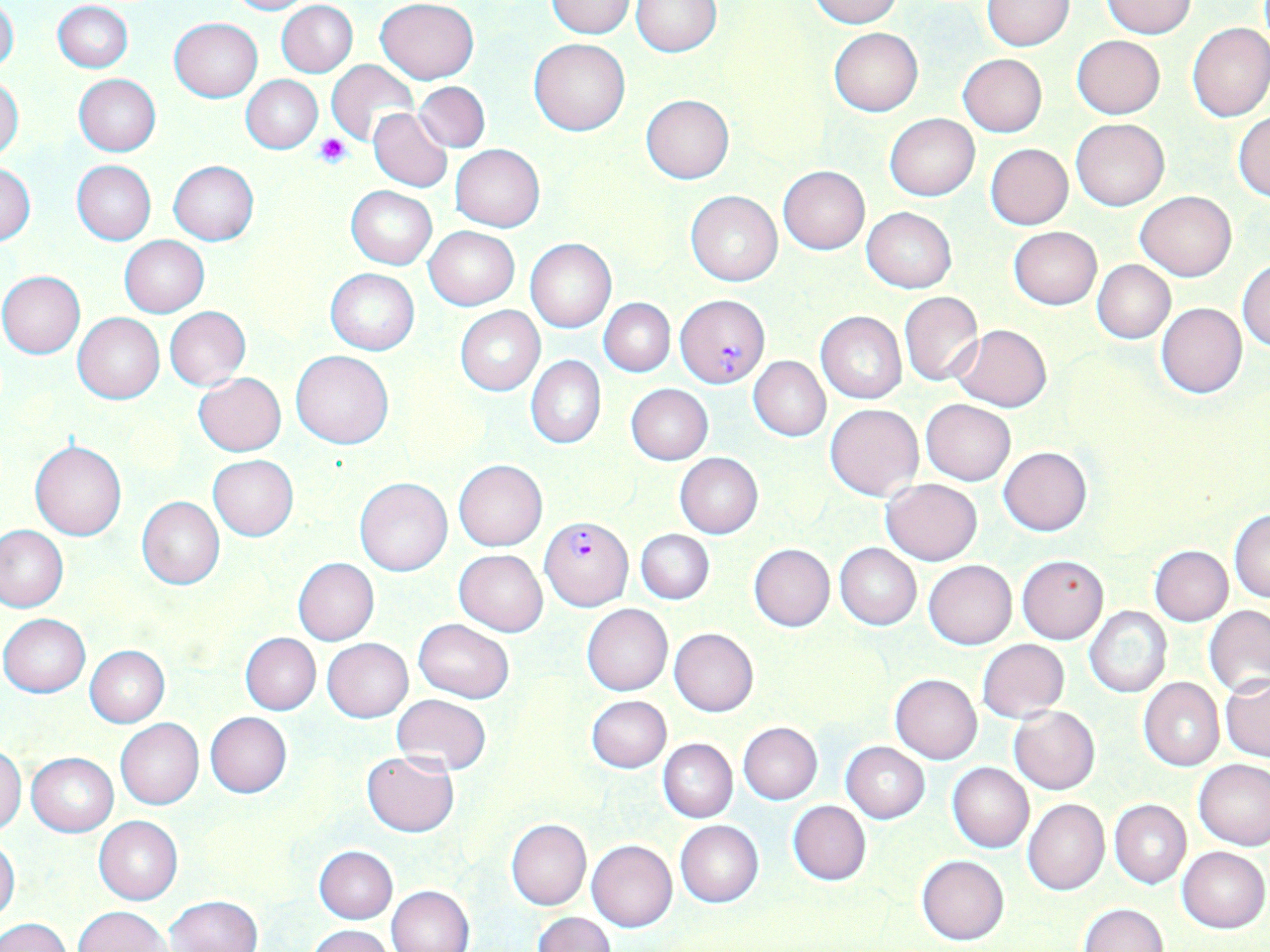

slide-level diagnosis = Plasmodium falciparum
modality = optical microscopy
magnification = 1000x
platelet locations = approximate bounding boxes as [x1, y1, x2, y2] in pixels: [314, 135, 350, 168]
image size = 1270×952 pixels
field of view = single
uninfected red blood cell locations = approximate bounding boxes as [x1, y1, x2, y2] in pixels: [226, 0, 310, 15], [375, 0, 479, 84], [808, 0, 901, 27], [981, 0, 1075, 50], [53, 1, 133, 73], [277, 1, 358, 77], [632, 1, 722, 55], [1101, 1, 1196, 38], [0, 2, 19, 76], [545, 2, 635, 37], [169, 18, 262, 101], [1186, 22, 1270, 121], [829, 27, 922, 117], [1071, 36, 1164, 118], [528, 38, 629, 135], [958, 54, 1047, 136], [326, 59, 418, 145], [73, 74, 160, 156], [242, 76, 322, 153], [0, 77, 24, 161], [415, 81, 490, 152], [641, 94, 733, 184], [368, 108, 452, 192], [1233, 112, 1270, 200], [884, 114, 979, 200], [1070, 116, 1169, 210], [450, 144, 544, 231], [985, 144, 1073, 229], [72, 160, 156, 244], [169, 160, 258, 245], [0, 163, 36, 245], [777, 166, 869, 254], [347, 185, 436, 269], [686, 191, 781, 286], [1135, 191, 1236, 280], [862, 207, 956, 292], [1008, 226, 1101, 309], [425, 227, 519, 309], [120, 237, 208, 316], [525, 240, 616, 332], [1236, 258, 1270, 352], [1091, 259, 1175, 343], [325, 268, 420, 355], [0, 271, 85, 358], [899, 291, 983, 385], [599, 299, 675, 376], [1156, 302, 1247, 399], [455, 306, 546, 396], [165, 307, 251, 389], [816, 311, 906, 403], [73, 312, 164, 404], [952, 324, 1051, 412], [292, 350, 394, 449], [526, 356, 606, 448], [749, 357, 830, 441], [194, 373, 286, 455], [627, 384, 713, 465], [921, 399, 1015, 485], [825, 403, 923, 501], [29, 439, 127, 540], [998, 446, 1091, 536], [674, 453, 762, 539], [208, 456, 298, 541], [453, 459, 548, 551], [354, 477, 453, 576], [880, 479, 982, 564], [137, 497, 224, 590], [1229, 510, 1270, 603], [0, 525, 67, 612], [636, 529, 714, 604], [748, 543, 834, 631], [834, 543, 921, 630], [1150, 545, 1233, 626], [455, 549, 547, 636], [1016, 556, 1108, 644], [294, 559, 379, 645], [924, 560, 1016, 648], [581, 604, 672, 696], [1204, 605, 1270, 698], [1085, 606, 1171, 698], [1, 614, 90, 697], [414, 618, 515, 702], [669, 627, 758, 716], [240, 632, 320, 715], [323, 638, 412, 722], [976, 640, 1069, 722], [85, 646, 170, 727], [889, 673, 983, 763], [1222, 674, 1270, 762], [1138, 677, 1224, 771], [392, 694, 491, 774], [586, 695, 671, 773], [1010, 706, 1100, 794], [206, 712, 291, 797], [116, 718, 203, 810], [738, 722, 822, 803], [657, 739, 737, 822], [841, 742, 930, 822], [0, 746, 25, 833], [26, 752, 118, 835], [361, 752, 458, 836], [1193, 758, 1270, 850], [947, 762, 1034, 852], [1023, 798, 1109, 895], [1110, 800, 1191, 888], [787, 801, 870, 886], [93, 817, 183, 904], [506, 819, 591, 909], [675, 820, 763, 907], [504, 829, 675, 919], [0, 839, 20, 925], [586, 840, 677, 931], [313, 845, 398, 922], [1177, 845, 1269, 932], [917, 855, 1010, 946], [388, 884, 474, 952], [167, 895, 263, 952], [1078, 902, 1167, 952], [76, 906, 169, 951], [534, 913, 615, 951], [0, 916, 72, 952], [306, 925, 394, 952]
stain = May-Grünwald-Giemsa
preparation = thin blood smear
Plasmodium falciparum-infected red blood cell locations = approximate bounding boxes as [x1, y1, x2, y2] in pixels: [675, 294, 771, 387], [540, 516, 633, 611]